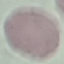 Malaria status: uninfected. Thin blood film. Photographed with a smartphone camera at the microscope eyepiece. Cell patch, automatically extracted from a larger field of view and resized to 64 × 64 pixels. Giemsa-stained preparation.